State the preparation type.
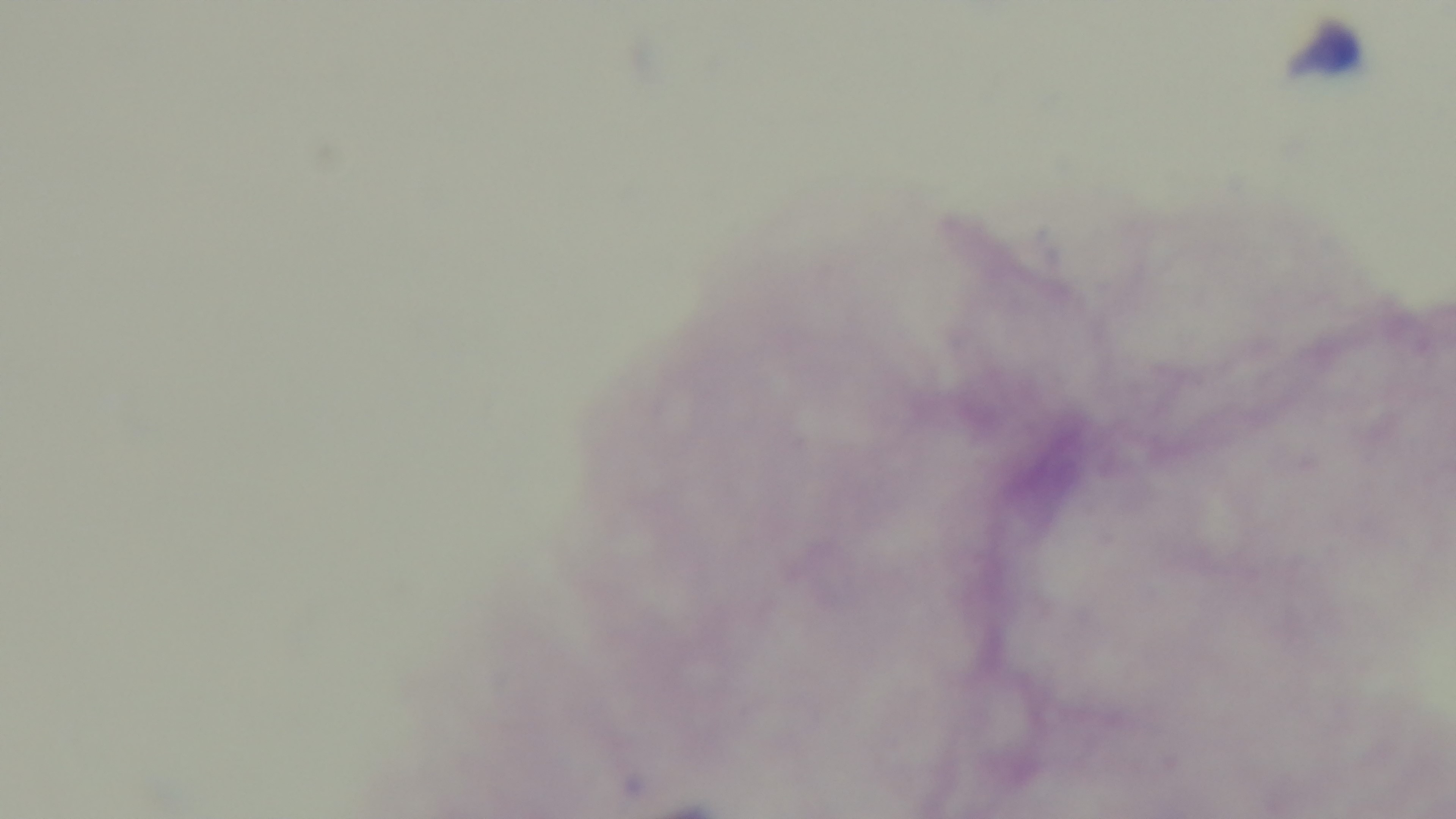

It is a thick blood film.

objective = 100x oil immersion
capture = mounted 4K digital camera
modality = light microscopy
malaria status = uninfected
stain = Giemsa
field of view = one from the slide